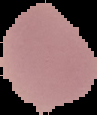

Summary:
  - Image type: cell region segmented out of the field of view; surrounding area masked to black
  - Image size: 97×115 pixels
  - Malaria status: uninfected
  - Preparation: thin blood film